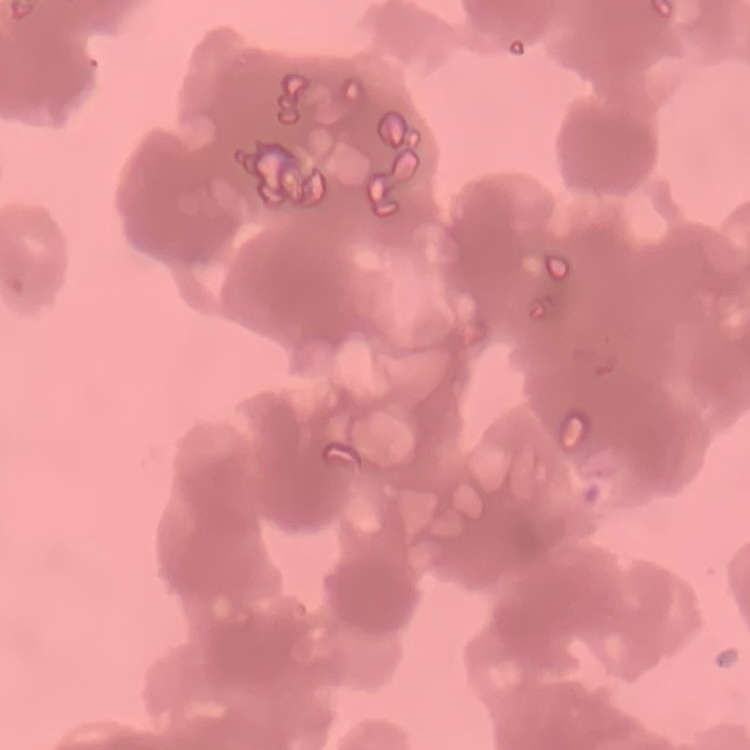
Summary:
  - Red blood cell morphology: rouleaux formation
  - Preparation: thin blood film
  - Image type: square crop of a larger photomicrograph
  - Stain: Field's or Giemsa